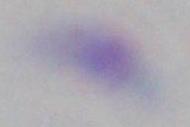
magnification = 1000x
identification = Toxoplasma gondii
modality = micrograph